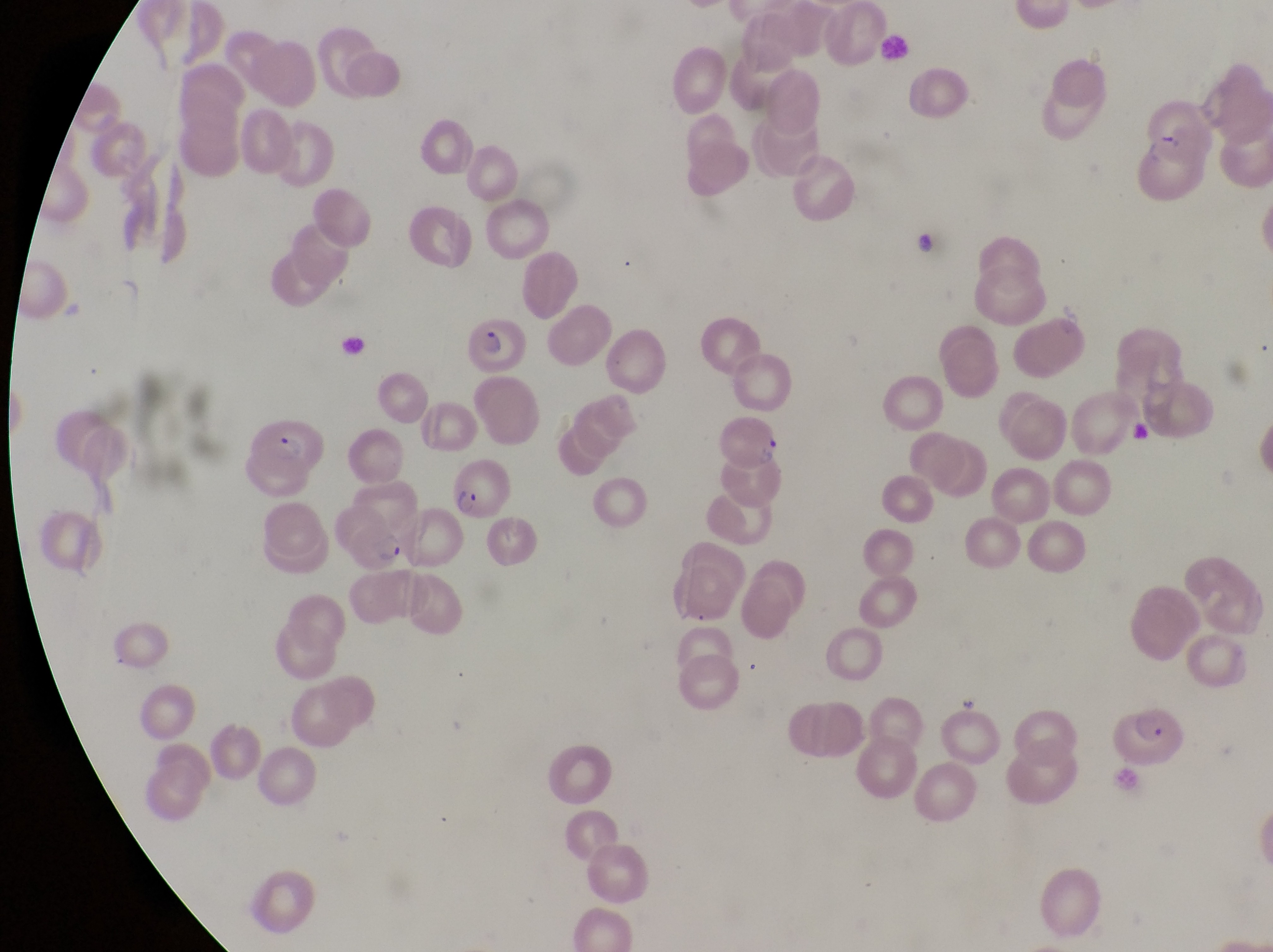 Approximate bounding boxes as {left, top, right, bottom} in pixels. Parasitised red blood cell locations: {460, 317, 525, 372}, {242, 407, 332, 485}, {717, 413, 782, 474}, {451, 465, 516, 525}, {332, 507, 410, 574}, {1115, 700, 1189, 765}. Single field of view. Image is 1273×952 pixels. Thin blood smear. Collected in Uganda. Captured by a smartphone held over the eyepiece of an Olympus CX-23 microscope. Magnification of 1000x.